Report the malaria status of this cell.
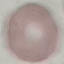

It is uninfected.

Summary:
  - Capture: smartphone through the microscope eyepiece
  - Stain: Giemsa
  - Image type: cell patch, automatically extracted from a larger field of view and resized to 64 × 64 pixels
  - Preparation: thin blood film